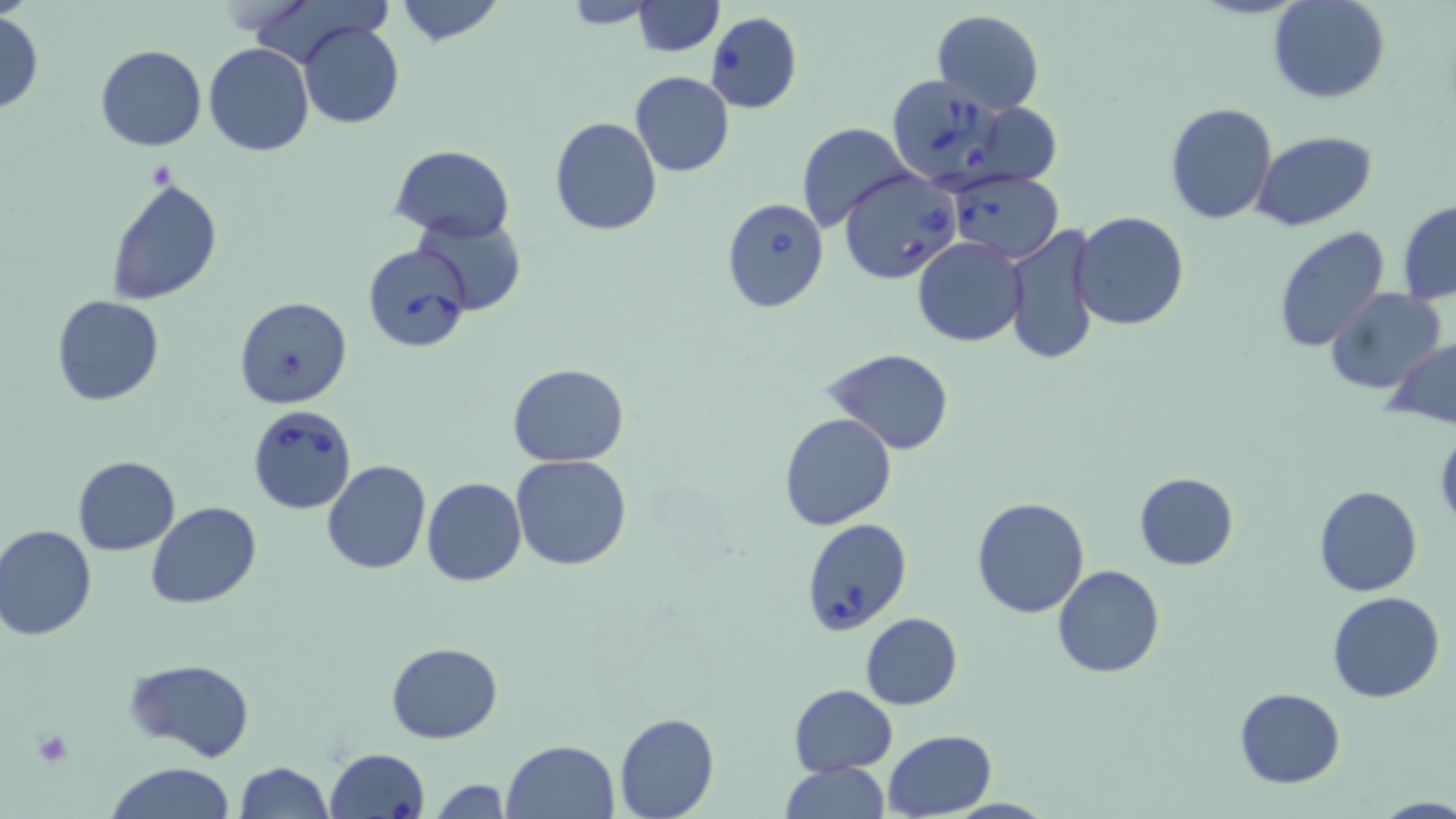
{
  "slide_level_diagnosis": "Babesia divergens",
  "preparation": "thin blood film",
  "uninfected_red_blood_cell_locations": "approximate bounding boxes as (x1,y1)-(x2,y2) corner pairs in pixels: (394,0)-(505,47), (632,0)-(723,55), (1268,0)-(1391,104), (560,1)-(659,28), (933,9)-(1043,112), (704,11)-(802,113), (0,12)-(43,113), (299,21)-(404,129), (204,41)-(314,158), (95,45)-(206,151), (629,71)-(735,176), (960,99)-(1069,186), (1164,101)-(1279,224), (549,117)-(662,237), (797,123)-(913,232), (1253,131)-(1377,233), (391,144)-(514,240), (103,173)-(224,307), (1398,200)-(1456,303), (1072,212)-(1189,329), (413,216)-(527,315), (1002,223)-(1102,365), (1273,225)-(1391,355), (913,236)-(1027,347), (1325,287)-(1449,396), (52,295)-(163,406), (232,295)-(353,409), (1383,336)-(1456,430), (824,349)-(956,455), (507,362)-(628,467), (779,412)-(897,531), (511,454)-(632,572), (72,455)-(181,554), (321,460)-(431,574), (1133,472)-(1239,569), (423,477)-(527,586), (1314,484)-(1423,598), (971,497)-(1091,619), (145,502)-(262,609), (0,525)-(97,641), (1051,565)-(1165,678), (1328,591)-(1443,702), (861,612)-(963,710), (387,641)-(502,743), (124,657)-(256,763), (788,683)-(897,777), (1234,687)-(1345,787), (613,711)-(719,819), (883,730)-(997,819), (501,739)-(619,819), (234,761)-(332,819), (105,762)-(237,819), (778,762)-(890,818), (428,777)-(512,817), (1375,797)-(1456,819)",
  "stain": "May-Grünwald-Giemsa",
  "platelet_locations": "approximate bounding boxes as (x1,y1)-(x2,y2) corner pairs in pixels: (31,731)-(74,767)",
  "babesia_divergens_infected_red_blood_cell_locations": "approximate bounding boxes as (x1,y1)-(x2,y2) corner pairs in pixels: (885,76)-(1011,188), (840,169)-(962,284), (947,172)-(1063,264), (721,197)-(829,312), (363,241)-(476,355), (246,405)-(357,515), (802,517)-(912,632), (326,747)-(429,819)",
  "modality": "light microscopy",
  "field_of_view": "single",
  "magnification": "1000x",
  "image_size": "1456×819 pixels"
}